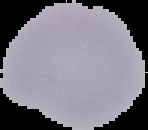
image size = 148×130 pixels
preparation = thin blood film
image type = cell region segmented out of the field of view; surrounding area masked to black
result = no malaria parasites detected